Locate and identify every blood parasite.
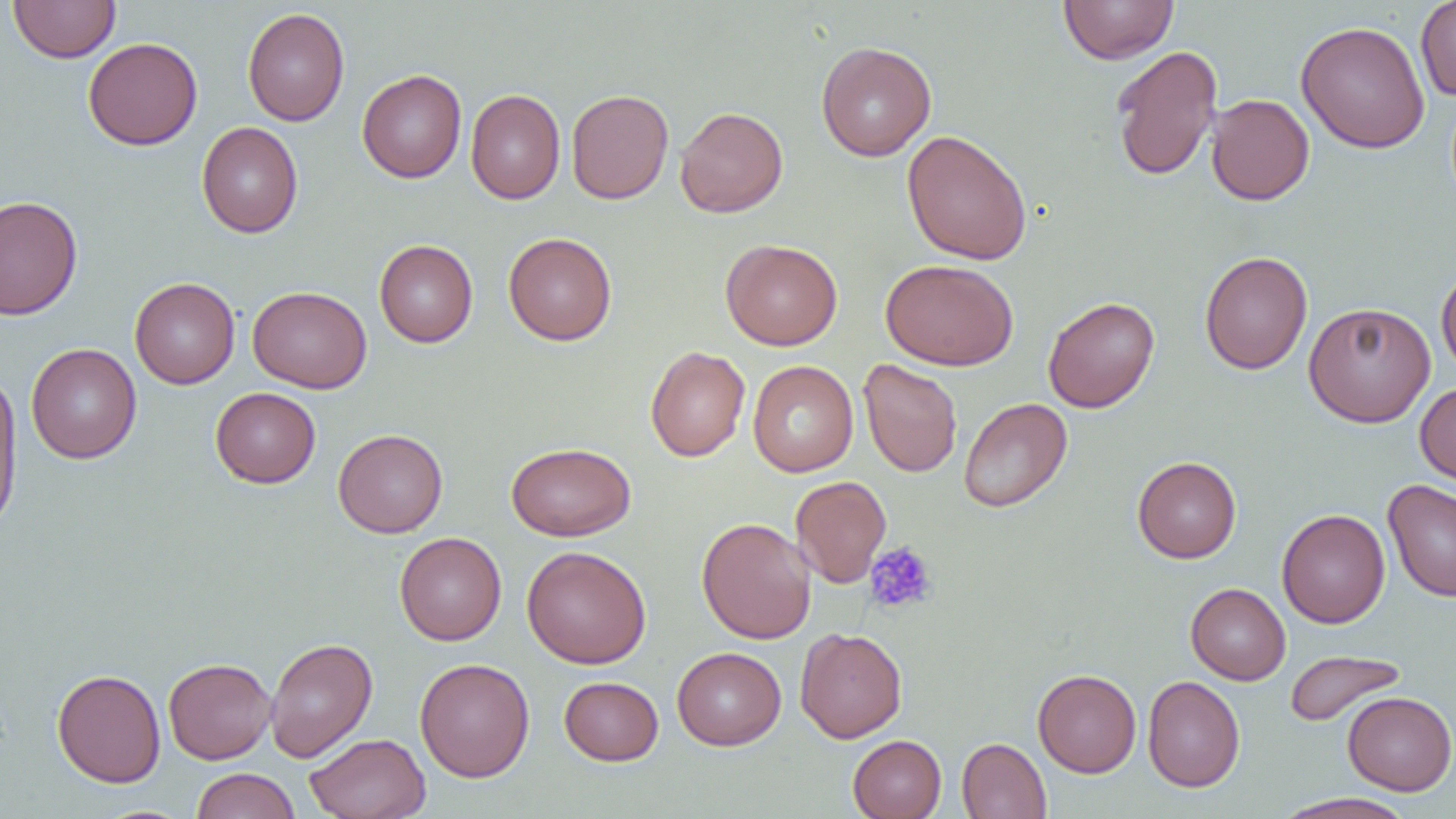
No blood parasites observed.

Summary:
  - Coordinate format: approximate bounding boxes as (x1,y1)-(x2,y2) corner pairs in pixels
  - Platelet locations: (864,541)-(938,615)
  - Uninfected red blood cell locations: (8,0)-(120,63), (1058,0)-(1178,64), (1415,0)-(1456,101), (242,7)-(349,126), (1295,20)-(1430,154), (83,37)-(202,151), (816,41)-(936,161), (1110,45)-(1223,182), (357,69)-(467,183), (465,89)-(565,204), (566,89)-(674,204), (1206,94)-(1315,205), (675,106)-(788,218), (197,122)-(302,238), (902,129)-(1033,265), (0,195)-(83,321), (503,232)-(617,345), (720,238)-(843,350), (374,240)-(478,347), (1199,250)-(1313,375), (880,259)-(1019,371), (1436,265)-(1456,378), (130,277)-(240,389), (247,286)-(372,393), (1043,296)-(1159,413), (1303,301)-(1436,427), (26,343)-(142,463), (645,346)-(750,462), (858,359)-(963,477), (747,360)-(859,477), (0,374)-(23,532), (1415,381)-(1456,488), (210,387)-(321,488), (958,397)-(1073,513), (333,428)-(448,538), (506,442)-(636,541), (1132,456)-(1242,563), (790,475)-(891,587), (1383,479)-(1455,602), (1277,508)-(1390,628), (696,517)-(816,644), (394,532)-(506,645), (521,545)-(651,669), (1186,583)-(1290,685), (795,627)-(907,743), (264,637)-(378,762), (672,647)-(786,750), (1284,649)-(1406,727), (163,658)-(277,764), (414,658)-(535,782), (52,668)-(166,787), (1032,669)-(1141,777), (1142,675)-(1245,792), (559,676)-(663,765), (1342,691)-(1455,795), (305,732)-(431,819), (847,735)-(946,818), (957,737)-(1051,819), (190,768)-(300,819), (1273,792)-(1419,819)
  - Slide-level diagnosis: no evidence of blood parasites
  - Field of view: one of a larger specimen
  - Magnification: 1000x
  - Image size: 1456×819 pixels
  - Preparation: thin blood film
  - Modality: optical microscopy